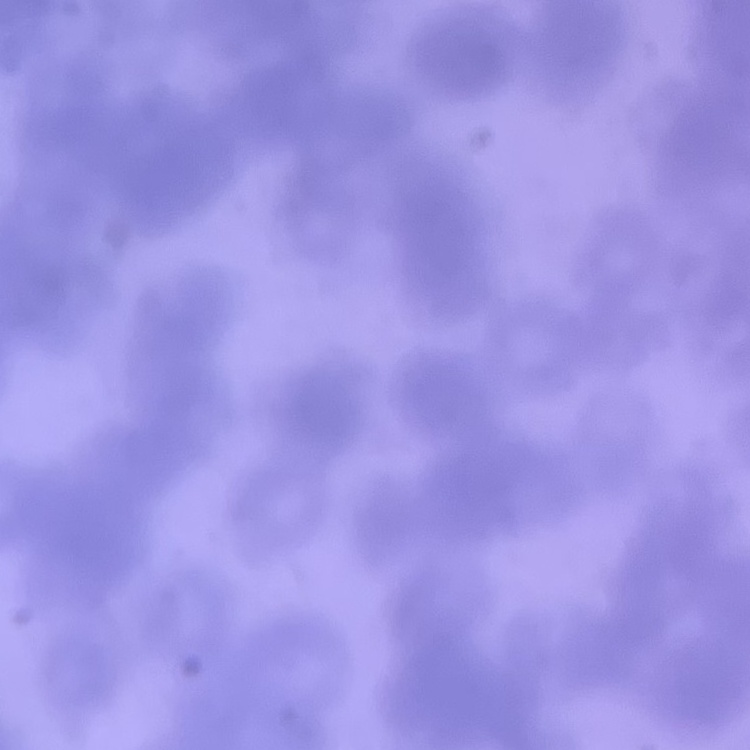
Summary:
  - Red blood cell morphology: rouleaux formation
  - Image type: one tile cut from a larger photomicrograph
  - Stain: Field's or Giemsa
  - Preparation: thin blood smear